Report the malaria status.
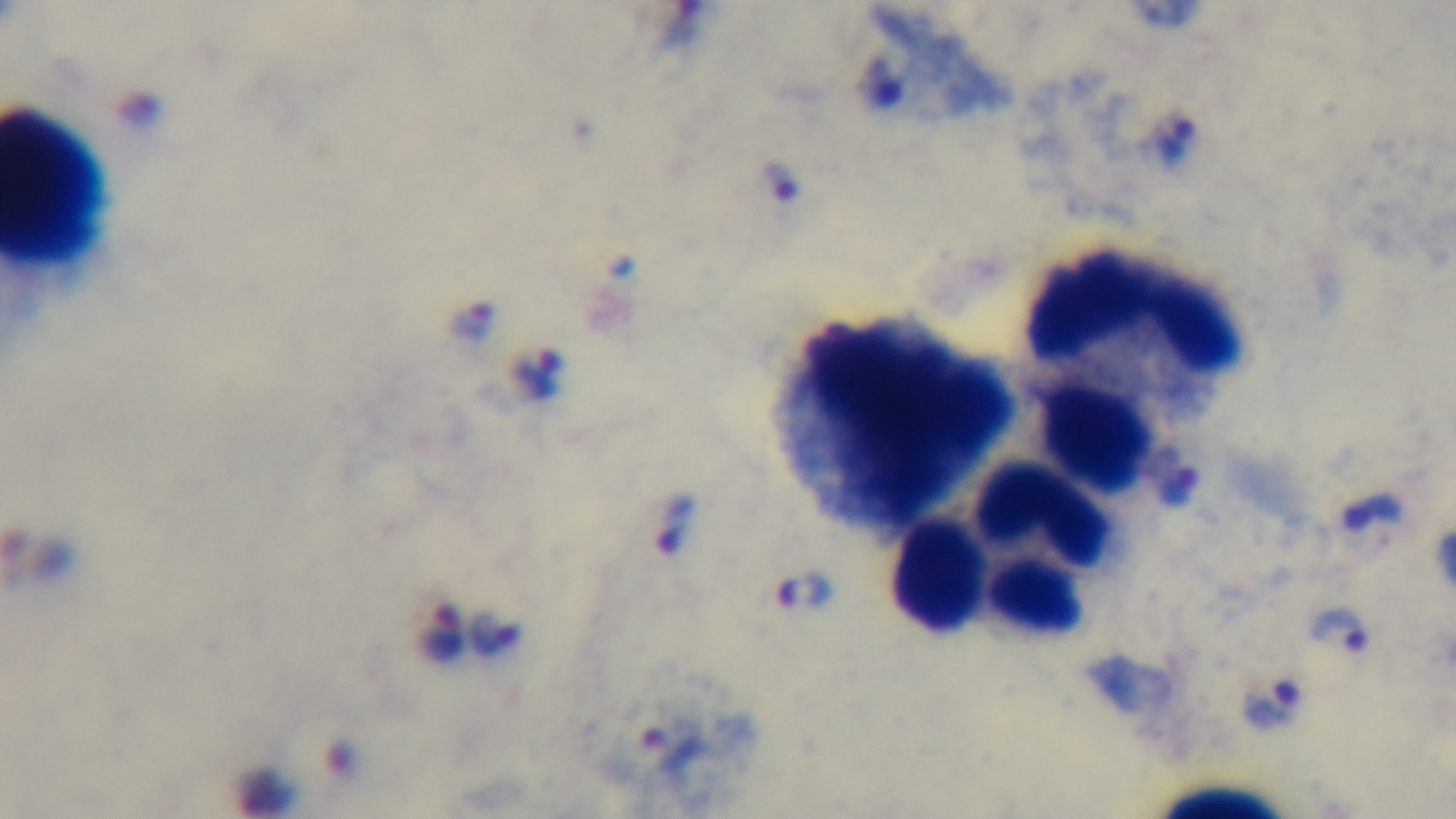

Positive.

{
  "stain": "Giemsa",
  "modality": "light microscopy",
  "capture": "mounted 4K digital camera",
  "objective": "100x oil immersion",
  "field_of_view": "one from the slide",
  "preparation": "thick smear"
}